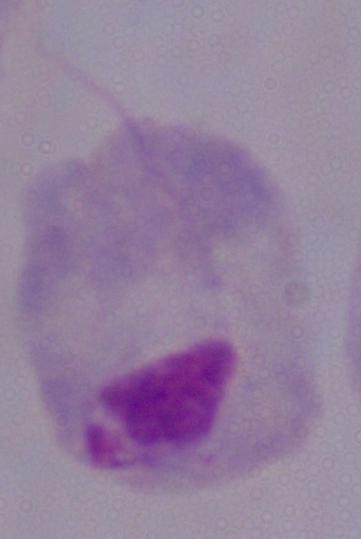

{
  "identification": "trichomonad",
  "magnification": "1000x",
  "modality": "photomicrograph"
}